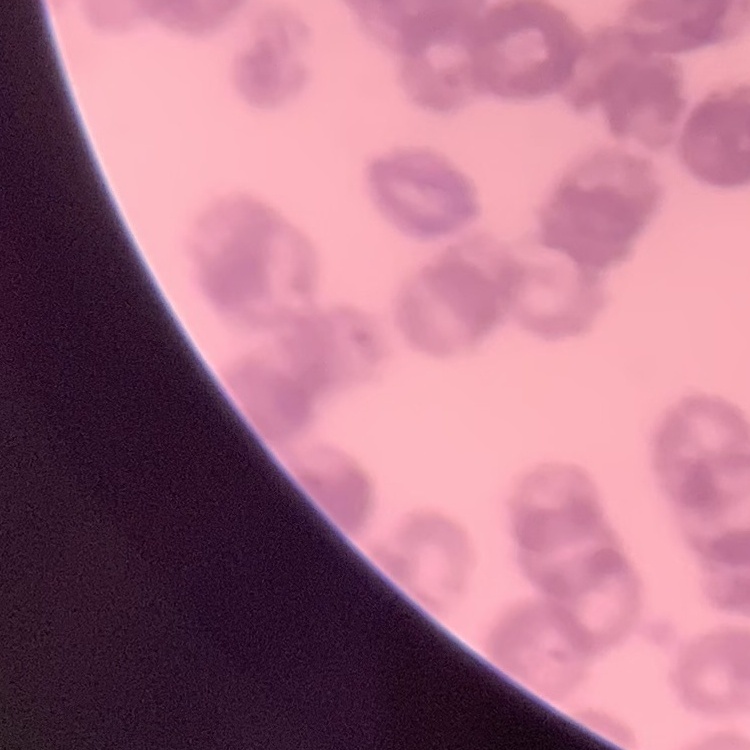 The erythrocytes show rouleaux formation. Field's or Giemsa stain. One tile cut from a larger photomicrograph. Thin blood film.